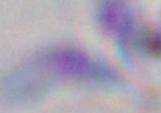

modality = photomicrograph
identification = Toxoplasma gondii
magnification = 1000x